Report the malaria status of this cell.
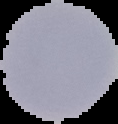

Uninfected.

Segmented cell region on a black background. Image is 118×124 pixels. From a thin blood smear.